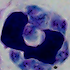
identification = white blood cell
modality = photomicrograph
magnification = 1000x